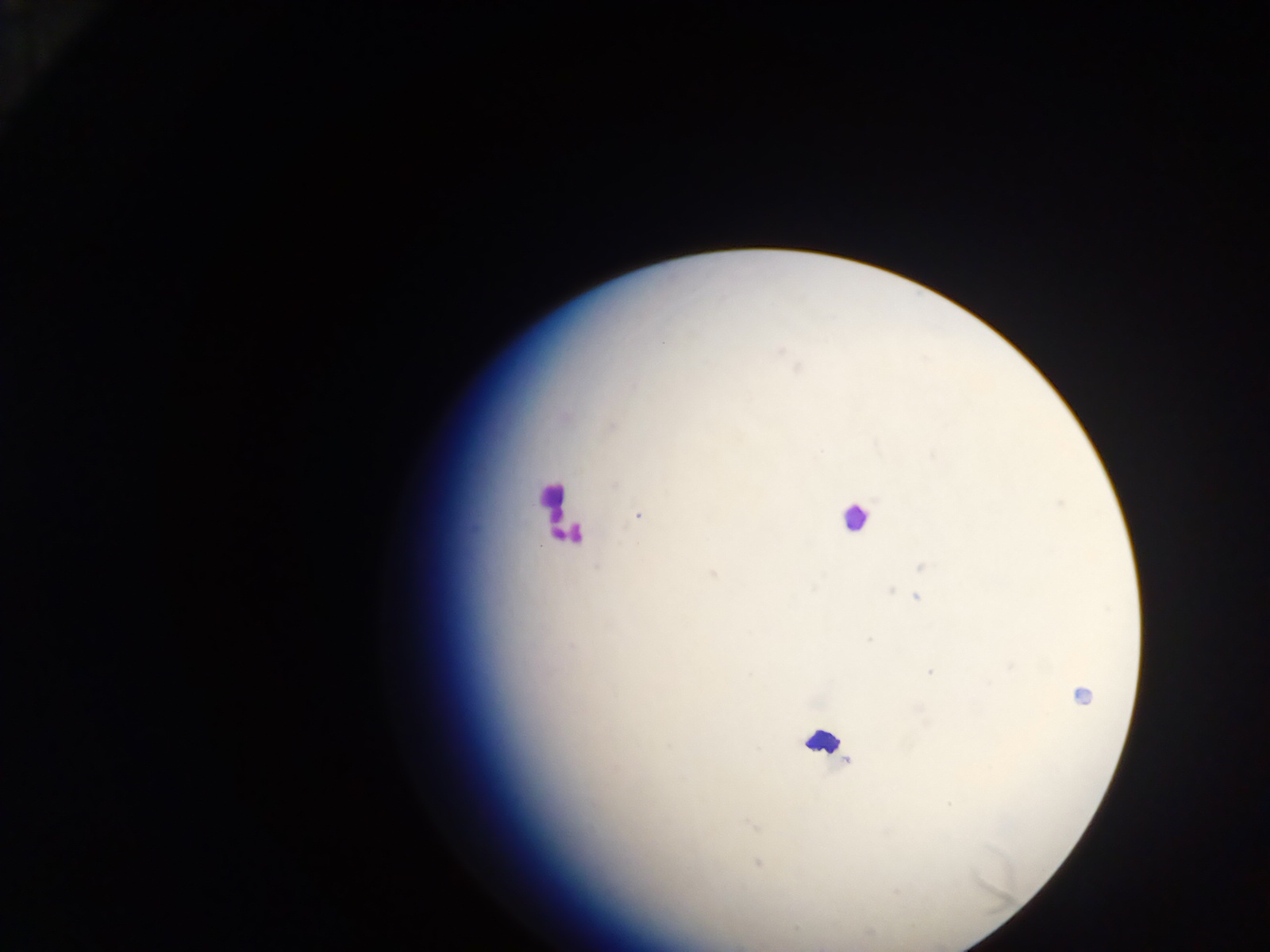
Approximate centers as [x, y] in pixels.
Summary:
  - Leukocyte locations: [553, 503], [855, 518], [570, 534], [823, 743]
  - Malaria parasite locations: [662, 342], [779, 351], [797, 367], [633, 385], [612, 426], [614, 485], [637, 515], [920, 566], [713, 574], [814, 588], [891, 590], [916, 597], [869, 640], [1011, 666], [930, 672], [1081, 695], [949, 803], [753, 825], [758, 864], [795, 928]
  - Capture: mobile-phone photograph through a microscope
  - Field of view: single
  - Country: Ghana
  - Preparation: thick blood film
  - Image size: 1270×952 pixels